Identify the parasite.
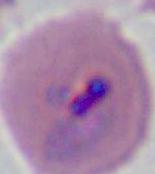
Plasmodium.

modality: micrograph
magnification: 400x or 1000x